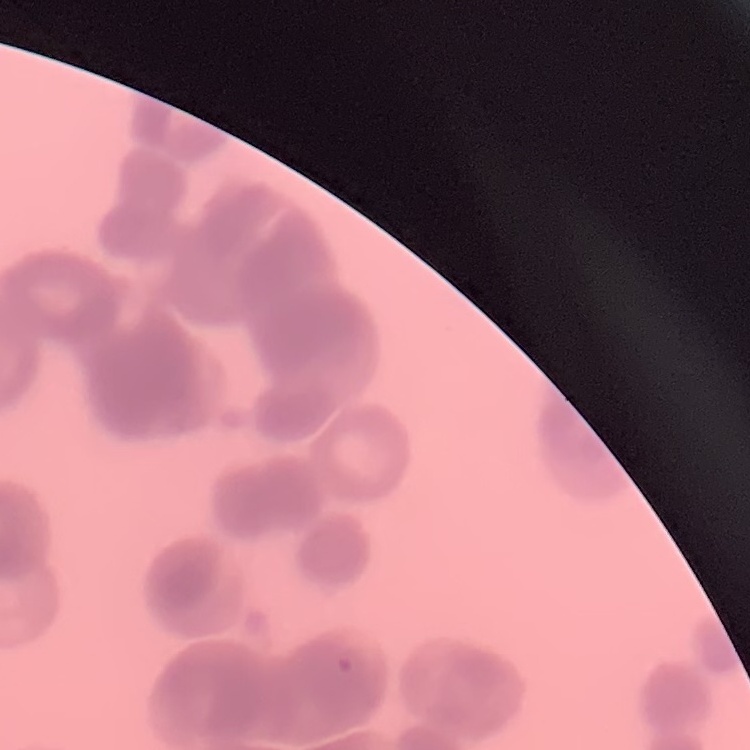
The erythrocytes show rouleaux formation. Field's or Giemsa stain. Thin blood smear. Square crop of a larger photomicrograph.